Point out every malaria parasite.
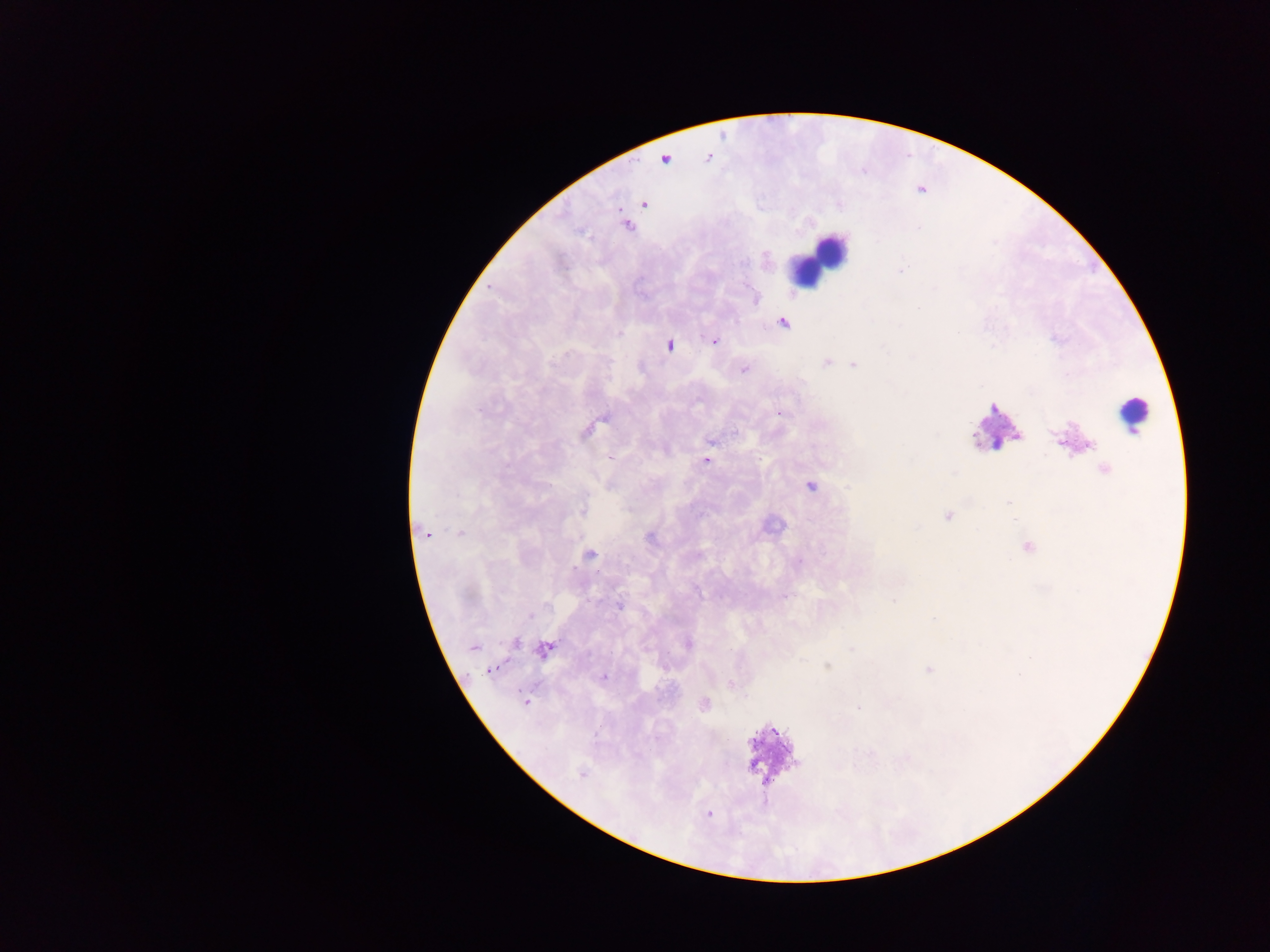

Approximate centers as x y in pixels.
Malaria parasites: 765 256; 900 271; 757 298; 918 309; 783 324; 718 342; 670 345; 826 362; 853 365; 744 369; 781 413; 602 420; 598 425; 588 433; 979 436; 710 442; 1061 443; 1088 444; 708 460; 1104 467; 810 486; 1008 503; 947 516; 460 533; 429 535; 649 538; 1027 547; 591 555; 786 597; 894 599; 619 606; 528 616; 932 617; 516 643; 687 644; 472 647; 851 647; 546 649; 543 654; 826 665; 488 670; 926 670; 607 677; 732 686; 526 701; 704 704; 859 709; 579 773.

leukocyte locations = approximate centers as x y in pixels: 823 252; 1134 408
field of view = single
preparation = thick blood film
image size = 1270×952 pixels
capture = mobile-phone photograph through a microscope
country = Ghana